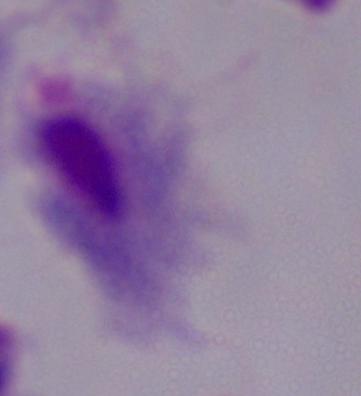
Photomicrograph. 1000x magnification. A trichomonad is shown.